State which cell type is depicted.
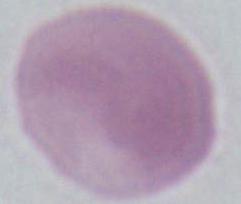

An erythrocyte.

Micrograph. 1000x magnification.